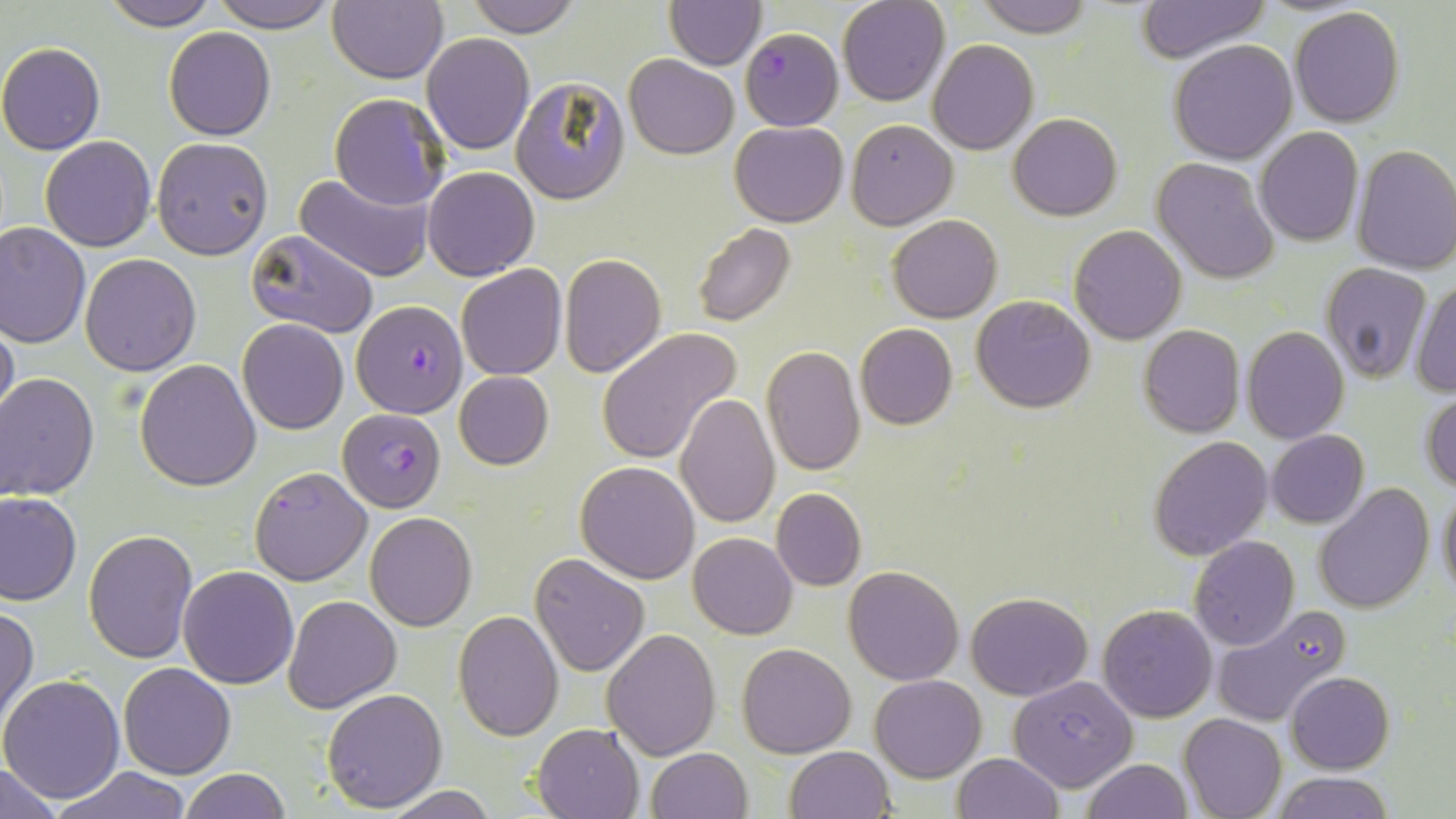
Approximate bounding boxes as [x1, y1, x2, y2] in pixels. Uninfected red blood cell locations: [98, 0, 218, 30], [210, 0, 343, 32], [329, 0, 447, 83], [462, 0, 580, 38], [665, 0, 765, 69], [837, 0, 950, 106], [973, 0, 1094, 38], [1133, 0, 1271, 63], [1288, 6, 1404, 127], [163, 27, 276, 141], [422, 32, 534, 154], [927, 39, 1039, 154], [1168, 39, 1298, 164], [0, 41, 106, 155], [625, 54, 739, 159], [510, 78, 630, 205], [329, 93, 451, 209], [1008, 112, 1122, 220], [730, 120, 848, 226], [846, 120, 957, 230], [1255, 127, 1364, 247], [40, 136, 156, 253], [152, 137, 274, 260], [1351, 144, 1456, 275], [1151, 157, 1280, 283], [422, 166, 540, 281], [296, 169, 436, 281], [888, 214, 1000, 322], [1, 222, 91, 349], [692, 222, 796, 328], [1069, 224, 1186, 345], [247, 230, 379, 339], [80, 253, 202, 375], [560, 253, 667, 376], [1320, 262, 1432, 384], [457, 264, 567, 380], [1409, 275, 1456, 399], [972, 295, 1095, 413], [1, 316, 18, 429], [239, 319, 348, 434], [855, 323, 958, 431], [1139, 324, 1245, 437], [1241, 327, 1349, 444], [597, 328, 741, 466], [761, 346, 864, 478], [134, 358, 261, 490], [453, 371, 554, 471], [1, 374, 99, 502], [1422, 392, 1456, 492], [675, 393, 781, 528], [1265, 430, 1368, 528], [1148, 435, 1273, 559], [576, 461, 699, 583], [1437, 484, 1456, 601], [1313, 486, 1434, 613], [771, 487, 867, 591], [1, 493, 81, 605], [365, 512, 477, 631], [83, 530, 199, 663], [688, 532, 797, 639], [1189, 537, 1300, 652], [530, 553, 649, 676], [844, 564, 964, 685], [178, 565, 299, 688], [966, 591, 1092, 700], [284, 595, 400, 712], [1099, 603, 1217, 722], [0, 605, 38, 729], [453, 609, 563, 741], [603, 628, 721, 758], [737, 642, 856, 758], [118, 662, 236, 779], [1287, 671, 1394, 773], [1, 674, 125, 804], [1009, 674, 1138, 791], [869, 675, 986, 782], [321, 688, 448, 812], [1179, 713, 1286, 819], [532, 722, 644, 818], [785, 746, 893, 819], [646, 747, 752, 819], [952, 753, 1061, 819], [1083, 759, 1192, 819], [0, 762, 65, 818], [53, 767, 193, 819], [179, 768, 289, 819], [1271, 772, 1396, 818], [380, 785, 499, 819]. Plasmodium falciparum-infected red blood cell locations: [740, 28, 842, 129], [351, 299, 468, 417], [337, 409, 446, 511], [249, 466, 373, 585], [1211, 603, 1351, 730]. Slide-level diagnosis: Plasmodium falciparum. May-Grünwald-Giemsa stain. Image is 1456×819 pixels. One field of a larger specimen. 1000x magnification. Optical microscopy. Thin blood film.